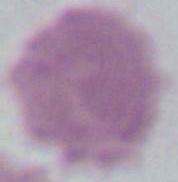
Micrograph. Captured at 1000x magnification. A red blood cell is seen.